State which cell type is depicted.
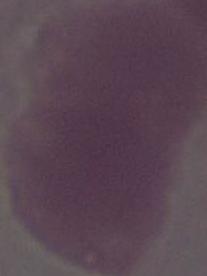

An erythrocyte.

magnification = 1000x
modality = photomicrograph